Assess this cell for malaria.
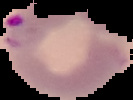

Parasitized.

preparation: thin blood film
image_size: 133×100 pixels
image_type: segmented cell region on a black background